Report the malaria status of this cell.
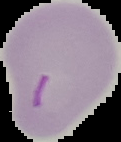

Parasitized.

Summary:
  - Image size: 121×142 pixels
  - Preparation: thin blood film
  - Image type: segmented cell region on a black background